Assess this cell for malaria.
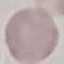

It is uninfected.

preparation = thin blood smear
image type = cell patch, automatically extracted from a larger field of view and resized to 64 × 64 pixels
capture = smartphone through the microscope eyepiece
stain = Giemsa